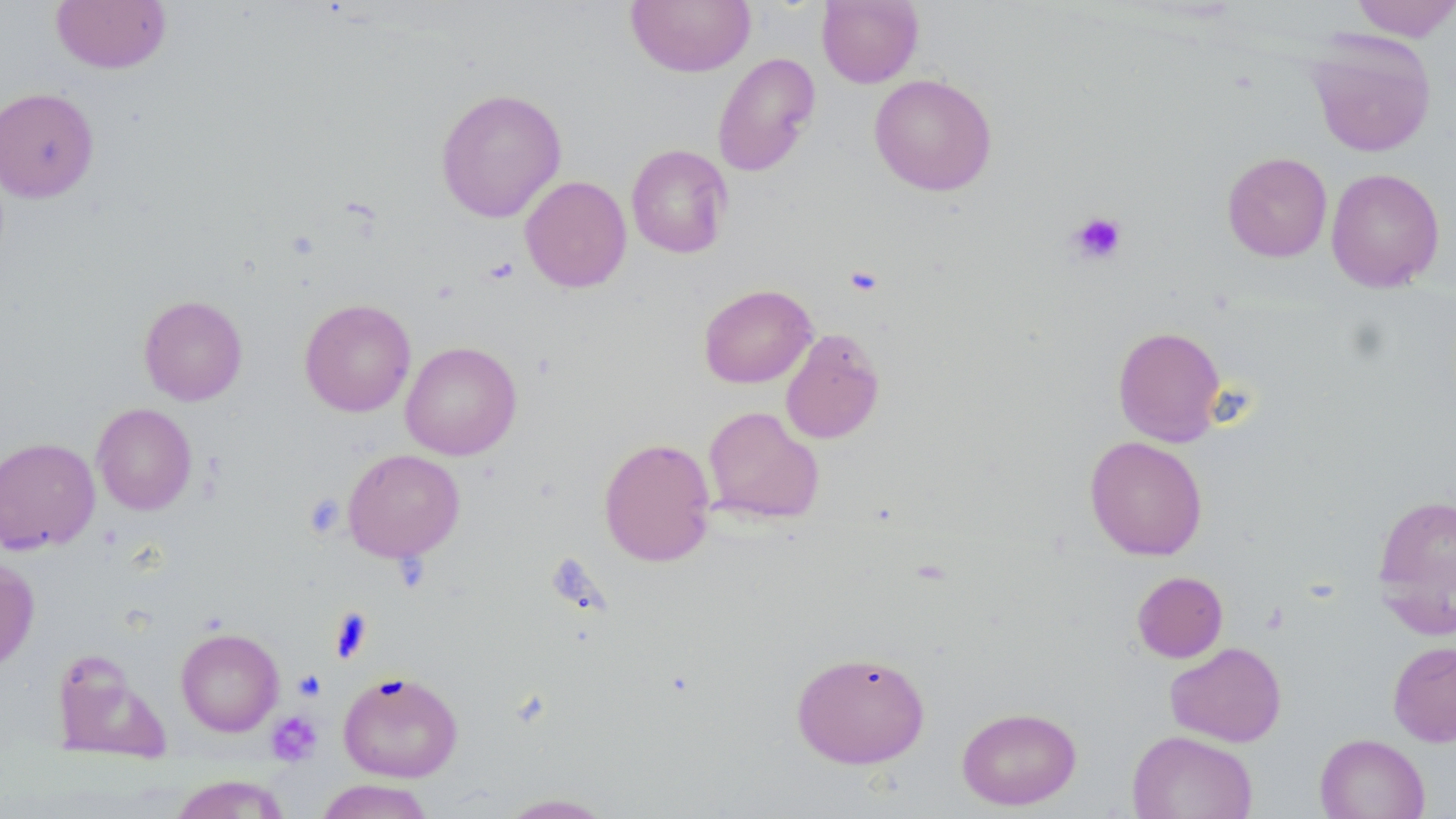
{
  "slide_level_diagnosis": "negative for blood parasites",
  "image_size": "1456×819 pixels",
  "stain": "May-Grünwald-Giemsa",
  "platelet_locations": "approximate bounding boxes as (x1,y1)-(x2,y2) corner pairs in pixels: (1068,211)-(1127,265), (844,265)-(883,296), (304,494)-(345,538), (330,607)-(374,662), (293,670)-(326,701), (266,711)-(322,765)",
  "magnification": "1000x",
  "uninfected_red_blood_cell_locations": "approximate bounding boxes as (x1,y1)-(x2,y2) corner pairs in pixels: (50,0)-(173,73), (625,0)-(756,77), (817,0)-(923,88), (1348,0)-(1456,41), (1305,31)-(1437,157), (712,52)-(820,177), (868,74)-(997,196), (0,87)-(99,202), (435,87)-(567,223), (626,144)-(733,259), (1222,152)-(1332,262), (1326,168)-(1445,292), (520,175)-(632,293), (699,284)-(817,388), (138,295)-(248,405), (299,298)-(416,417), (1112,325)-(1226,446), (781,328)-(885,444), (400,341)-(522,460), (92,403)-(197,515), (702,405)-(824,525), (1084,436)-(1208,561), (0,437)-(100,554), (598,437)-(716,567), (343,449)-(465,561), (1372,492)-(1456,632), (0,557)-(39,673), (1132,571)-(1228,662), (175,628)-(284,736), (1387,641)-(1456,747), (1165,642)-(1287,747), (790,650)-(930,769), (53,653)-(168,762), (338,670)-(463,782), (957,706)-(1081,810), (1127,730)-(1258,819), (1315,733)-(1429,819), (169,774)-(290,819), (315,778)-(435,819), (495,792)-(616,818)",
  "field_of_view": "single",
  "modality": "optical microscopy",
  "preparation": "thin blood smear"
}